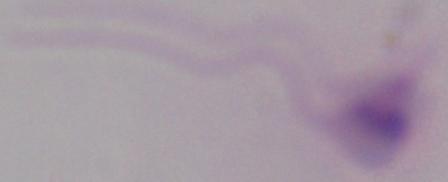
modality = photomicrograph
magnification = 1000x
identification = Leishmania